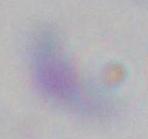
1000x magnification. Photomicrograph. Toxoplasma gondii is shown.